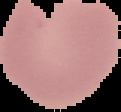

malaria_status: parasitized
image_type: cell region segmented out of the field of view; surrounding area masked to black
preparation: thin blood film
image_size: 121×112 pixels